Identify the parasite.
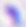

Toxoplasma gondii.

Captured at 400x magnification. Photomicrograph.